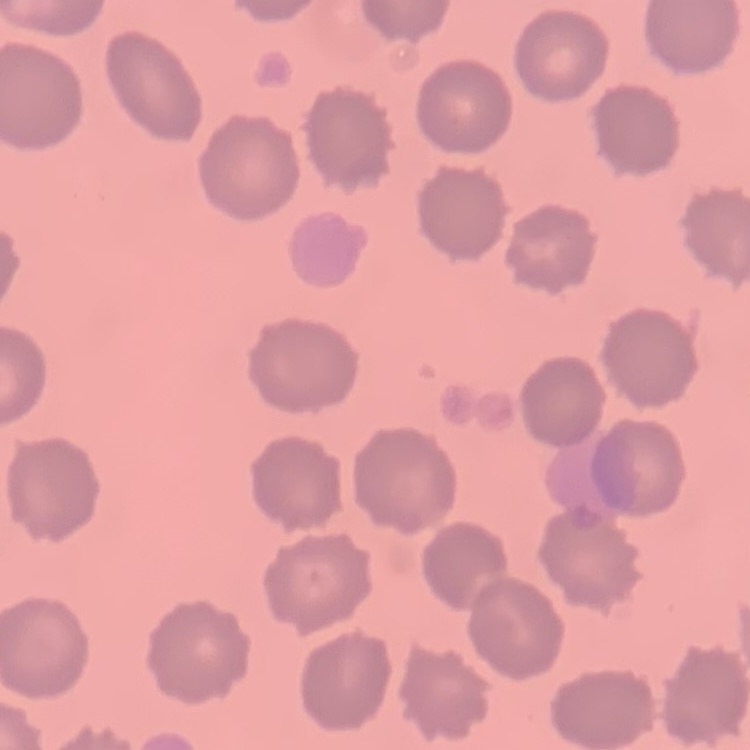
The erythrocytes exhibit no rouleaux formation. Thin blood film. Stained with either Field's or Giemsa. Square crop of a larger photomicrograph.